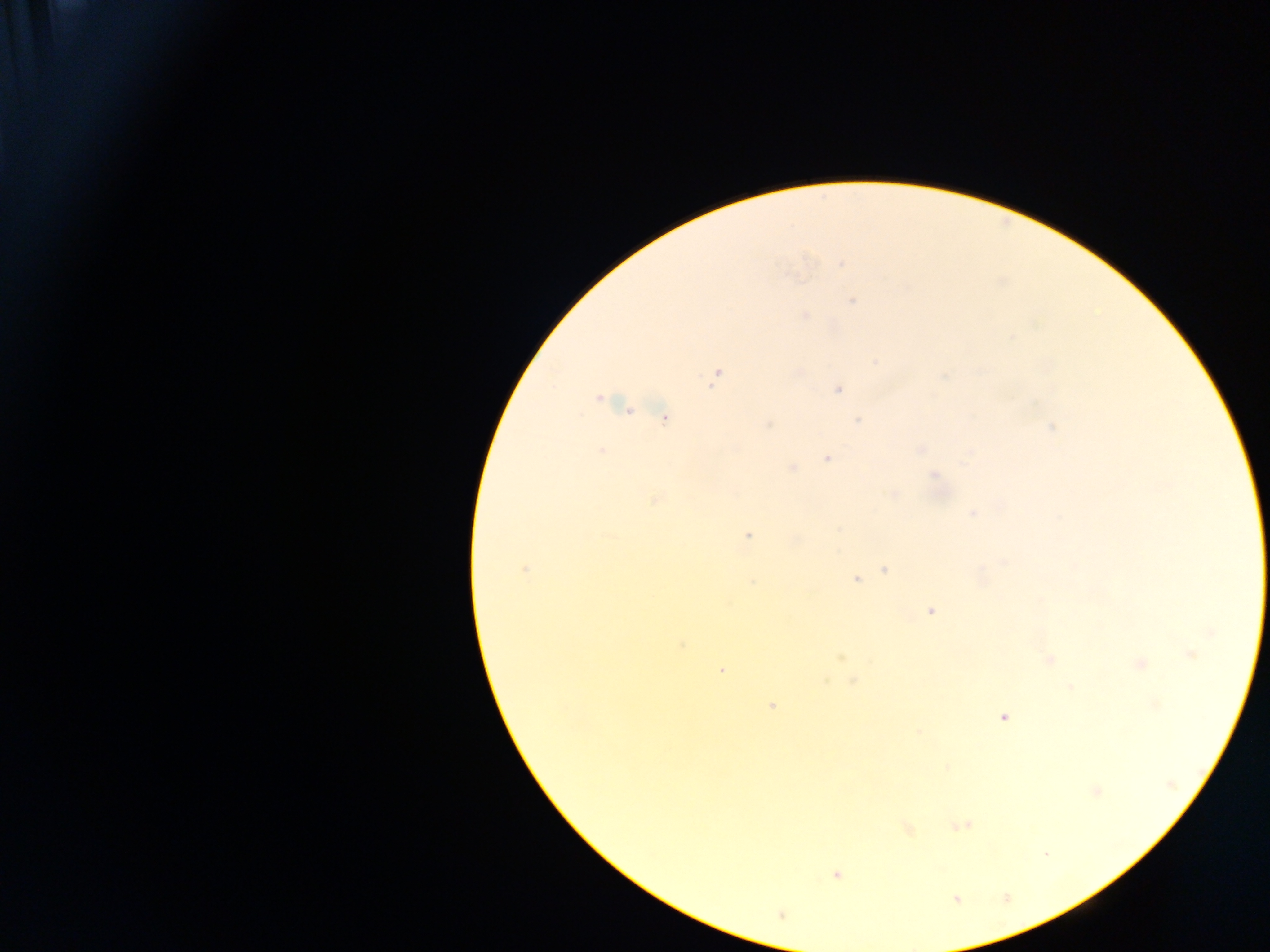

{
  "capture": "mobile-phone photograph through a microscope",
  "field_of_view": "single",
  "malaria_parasite_locations": "approximate centers as x y in pixels: 842 264; 852 302; 805 315; 876 362; 715 375; 838 389; 598 399; 664 418; 859 420; 768 425; 1052 427; 920 449; 601 451; 969 454; 827 458; 791 468; 934 476; 892 494; 654 499; 972 513; 1058 517; 748 535; 1004 563; 525 570; 884 570; 856 579; 753 582; 931 611; 1211 632; 683 645; 1190 655; 840 658; 1049 660; 1139 664; 721 670; 852 680; 1070 688; 772 706; 1004 717; 919 731; 1096 791; 961 825; 908 828; 1045 854; 836 875",
  "country": "Ghana",
  "preparation": "thick blood smear",
  "image_size": "1270×952 pixels"
}